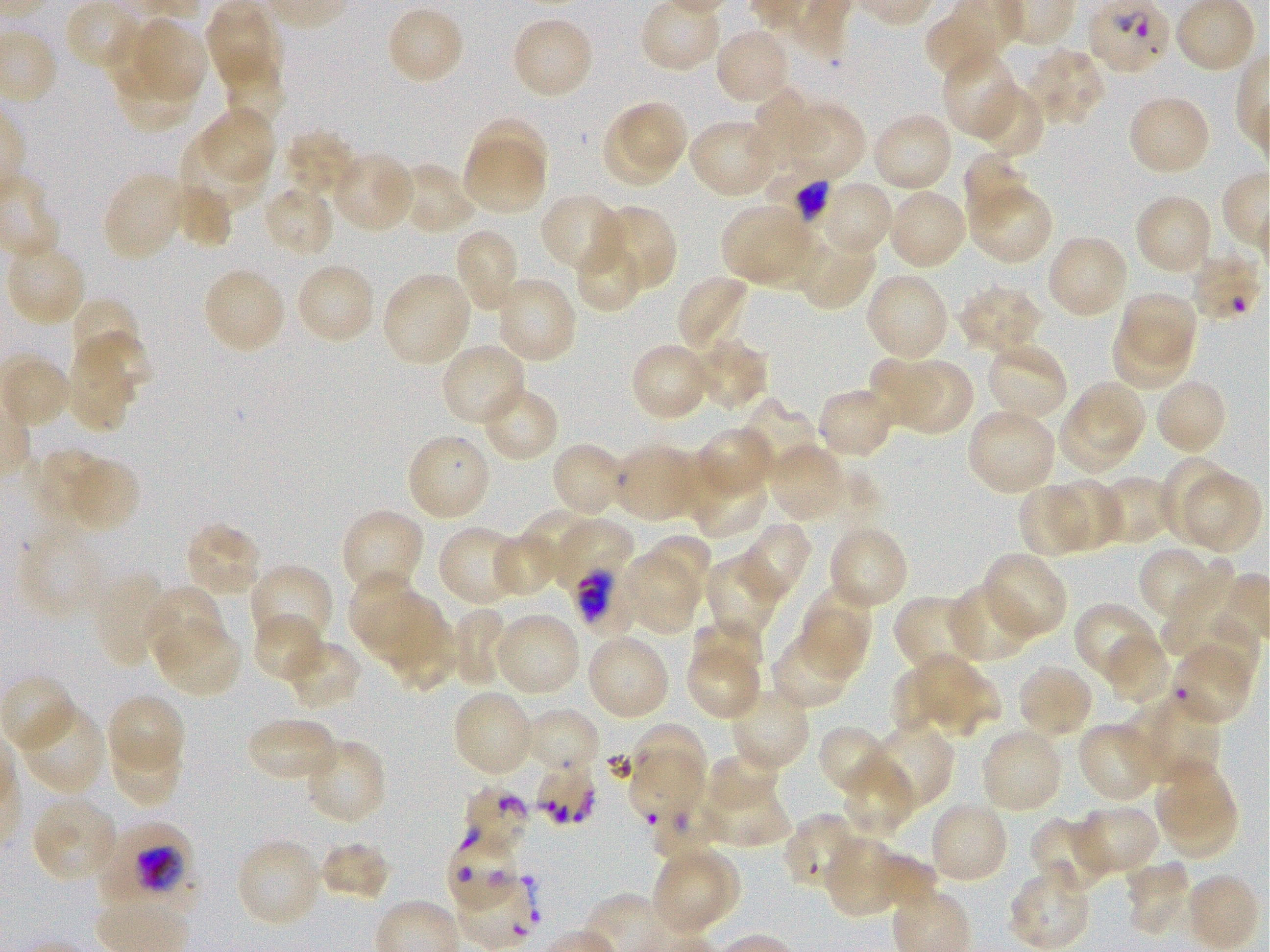
Not every red blood cell is marked. A life-cycle stage — or a range of stages, where the recorded stages span more than one — follows each staged infected red blood cell.
locations_of_uninfected_red_blood_cells: 'approximate bounding rectangles given as corner coordinates in pixels from the top-left: (x1=206, y1=0, x2=283, y2=92), (x1=924, y1=0, x2=1019, y2=83), (x1=386, y1=5, x2=466, y2=85), (x1=137, y1=16, x2=206, y2=98), (x1=510, y1=16, x2=594, y2=100), (x1=713, y1=27, x2=792, y2=106), (x1=1026, y1=47, x2=1107, y2=129), (x1=942, y1=51, x2=1023, y2=141), (x1=110, y1=62, x2=200, y2=133), (x1=223, y1=69, x2=288, y2=126), (x1=972, y1=82, x2=1046, y2=160), (x1=746, y1=88, x2=833, y2=170), (x1=1127, y1=94, x2=1212, y2=177), (x1=781, y1=101, x2=866, y2=184), (x1=619, y1=103, x2=687, y2=168), (x1=202, y1=107, x2=276, y2=182), (x1=601, y1=111, x2=677, y2=187), (x1=870, y1=112, x2=954, y2=193), (x1=472, y1=115, x2=549, y2=189), (x1=687, y1=118, x2=781, y2=200), (x1=284, y1=129, x2=355, y2=192), (x1=182, y1=132, x2=264, y2=207), (x1=462, y1=136, x2=549, y2=215), (x1=332, y1=151, x2=415, y2=233), (x1=963, y1=151, x2=1033, y2=226), (x1=394, y1=162, x2=476, y2=236), (x1=102, y1=170, x2=188, y2=262), (x1=170, y1=180, x2=234, y2=248), (x1=967, y1=180, x2=1052, y2=265), (x1=826, y1=185, x2=891, y2=250), (x1=262, y1=187, x2=331, y2=254), (x1=887, y1=188, x2=969, y2=271), (x1=539, y1=193, x2=629, y2=277), (x1=1134, y1=193, x2=1215, y2=276), (x1=720, y1=202, x2=807, y2=281), (x1=594, y1=203, x2=677, y2=292), (x1=740, y1=224, x2=825, y2=293), (x1=453, y1=228, x2=520, y2=313), (x1=799, y1=233, x2=877, y2=310), (x1=1046, y1=233, x2=1129, y2=321), (x1=573, y1=234, x2=645, y2=313), (x1=5, y1=240, x2=87, y2=328), (x1=293, y1=262, x2=377, y2=346), (x1=202, y1=266, x2=287, y2=356), (x1=381, y1=270, x2=474, y2=367), (x1=863, y1=271, x2=951, y2=362), (x1=676, y1=274, x2=750, y2=354), (x1=494, y1=276, x2=577, y2=365), (x1=956, y1=284, x2=1044, y2=355), (x1=1117, y1=293, x2=1197, y2=371), (x1=73, y1=297, x2=142, y2=362), (x1=1109, y1=323, x2=1189, y2=394), (x1=73, y1=331, x2=156, y2=387), (x1=687, y1=338, x2=768, y2=411), (x1=984, y1=340, x2=1069, y2=423), (x1=440, y1=342, x2=527, y2=427), (x1=630, y1=342, x2=712, y2=422), (x1=65, y1=345, x2=135, y2=434), (x1=872, y1=357, x2=944, y2=427), (x1=902, y1=359, x2=973, y2=435), (x1=1153, y1=377, x2=1228, y2=455), (x1=1073, y1=380, x2=1148, y2=452), (x1=479, y1=383, x2=560, y2=463), (x1=817, y1=386, x2=898, y2=460), (x1=739, y1=397, x2=822, y2=477), (x1=966, y1=407, x2=1058, y2=496), (x1=1055, y1=408, x2=1141, y2=478), (x1=694, y1=426, x2=775, y2=500), (x1=405, y1=432, x2=493, y2=523), (x1=550, y1=441, x2=627, y2=519), (x1=768, y1=442, x2=848, y2=523), (x1=611, y1=443, x2=704, y2=523), (x1=30, y1=447, x2=98, y2=532), (x1=58, y1=454, x2=141, y2=534), (x1=1160, y1=455, x2=1234, y2=546), (x1=684, y1=462, x2=768, y2=538), (x1=1183, y1=472, x2=1262, y2=555), (x1=1101, y1=475, x2=1172, y2=540), (x1=1049, y1=480, x2=1122, y2=552), (x1=1017, y1=483, x2=1094, y2=557), (x1=340, y1=508, x2=425, y2=596), (x1=523, y1=508, x2=598, y2=582), (x1=565, y1=517, x2=631, y2=587), (x1=732, y1=521, x2=811, y2=605), (x1=183, y1=522, x2=264, y2=599), (x1=437, y1=525, x2=524, y2=605), (x1=827, y1=525, x2=908, y2=611), (x1=13, y1=532, x2=108, y2=627), (x1=489, y1=532, x2=563, y2=598), (x1=641, y1=532, x2=712, y2=604), (x1=1137, y1=545, x2=1209, y2=617), (x1=619, y1=547, x2=705, y2=635), (x1=981, y1=552, x2=1068, y2=642), (x1=1160, y1=553, x2=1234, y2=655), (x1=704, y1=558, x2=780, y2=637), (x1=249, y1=563, x2=335, y2=649), (x1=93, y1=571, x2=169, y2=666), (x1=348, y1=573, x2=416, y2=641), (x1=144, y1=584, x2=224, y2=665), (x1=946, y1=584, x2=1037, y2=664), (x1=797, y1=589, x2=872, y2=682), (x1=893, y1=594, x2=981, y2=677), (x1=362, y1=597, x2=444, y2=662), (x1=1074, y1=601, x2=1159, y2=686), (x1=450, y1=606, x2=513, y2=688), (x1=492, y1=611, x2=582, y2=697), (x1=1183, y1=612, x2=1259, y2=687), (x1=251, y1=613, x2=325, y2=684), (x1=153, y1=617, x2=243, y2=698), (x1=391, y1=624, x2=454, y2=692), (x1=692, y1=624, x2=762, y2=673), (x1=1103, y1=630, x2=1173, y2=706), (x1=585, y1=632, x2=671, y2=721), (x1=770, y1=633, x2=855, y2=711), (x1=282, y1=641, x2=363, y2=713), (x1=686, y1=650, x2=762, y2=721), (x1=919, y1=654, x2=999, y2=738), (x1=890, y1=659, x2=943, y2=732), (x1=1015, y1=664, x2=1094, y2=739), (x1=728, y1=686, x2=810, y2=773), (x1=456, y1=689, x2=537, y2=774), (x1=106, y1=693, x2=186, y2=769), (x1=1148, y1=696, x2=1220, y2=782), (x1=1118, y1=702, x2=1189, y2=781), (x1=18, y1=705, x2=106, y2=794), (x1=524, y1=708, x2=598, y2=763), (x1=1077, y1=721, x2=1163, y2=803), (x1=246, y1=722, x2=334, y2=777), (x1=626, y1=722, x2=707, y2=796), (x1=864, y1=723, x2=953, y2=813), (x1=817, y1=725, x2=897, y2=798), (x1=979, y1=728, x2=1064, y2=814), (x1=116, y1=738, x2=180, y2=806), (x1=302, y1=738, x2=386, y2=826), (x1=706, y1=754, x2=779, y2=806), (x1=633, y1=755, x2=702, y2=819), (x1=843, y1=755, x2=916, y2=840), (x1=1152, y1=757, x2=1232, y2=834), (x1=1165, y1=794, x2=1238, y2=858), (x1=29, y1=795, x2=119, y2=885), (x1=701, y1=797, x2=791, y2=845), (x1=928, y1=800, x2=1010, y2=885), (x1=1074, y1=803, x2=1161, y2=879), (x1=1030, y1=817, x2=1113, y2=898), (x1=823, y1=834, x2=906, y2=917), (x1=235, y1=837, x2=323, y2=928), (x1=318, y1=840, x2=391, y2=900), (x1=662, y1=845, x2=740, y2=917), (x1=655, y1=854, x2=725, y2=935), (x1=1123, y1=859, x2=1192, y2=939), (x1=1007, y1=867, x2=1091, y2=950), (x1=1184, y1=872, x2=1260, y2=951), (x1=452, y1=874, x2=539, y2=947)'
locations_of_infected_red_blood_cells: 'approximate bounding rectangles given as corner coordinates in pixels from the top-left: (x1=766, y1=170, x2=847, y2=229); (x1=568, y1=563, x2=639, y2=637) late trophozoite; (x1=99, y1=820, x2=196, y2=908) trophozoite'
donor_blood_group: O+
preparation: thin blood smear
image_size: 1270×952 pixels
culture: static in-vitro Plasmodium falciparum strain 3D7
field_of_view: single
objective: 100x, oil immersion, numerical aperture 1.25
stain: Giemsa
locations_of_red_blood_cells_of_indeterminate_infection_status: 'approximate bounding rectangles given as corner coordinates in pixels from the top-left: (x1=1191, y1=254, x2=1258, y2=321), (x1=1170, y1=645, x2=1255, y2=725), (x1=532, y1=763, x2=600, y2=820), (x1=464, y1=782, x2=530, y2=851), (x1=651, y1=798, x2=729, y2=859), (x1=782, y1=813, x2=862, y2=888), (x1=446, y1=839, x2=522, y2=914)'